Describe the morphology of the erythrocytes.
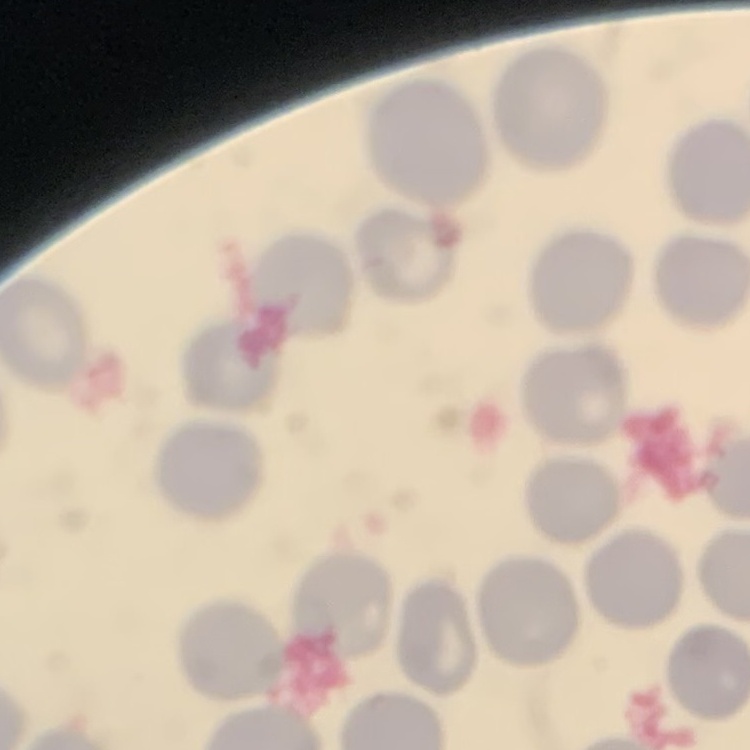

They show no rouleaux formation.

Stained with either Field's or Giemsa. Square crop of a larger photomicrograph. Thin blood film.